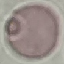
result = no malaria parasites seen
stain = Giemsa
preparation = thin smear
image type = automatically extracted cell patch, resized to 64 × 64 pixels
capture = smartphone through the microscope eyepiece